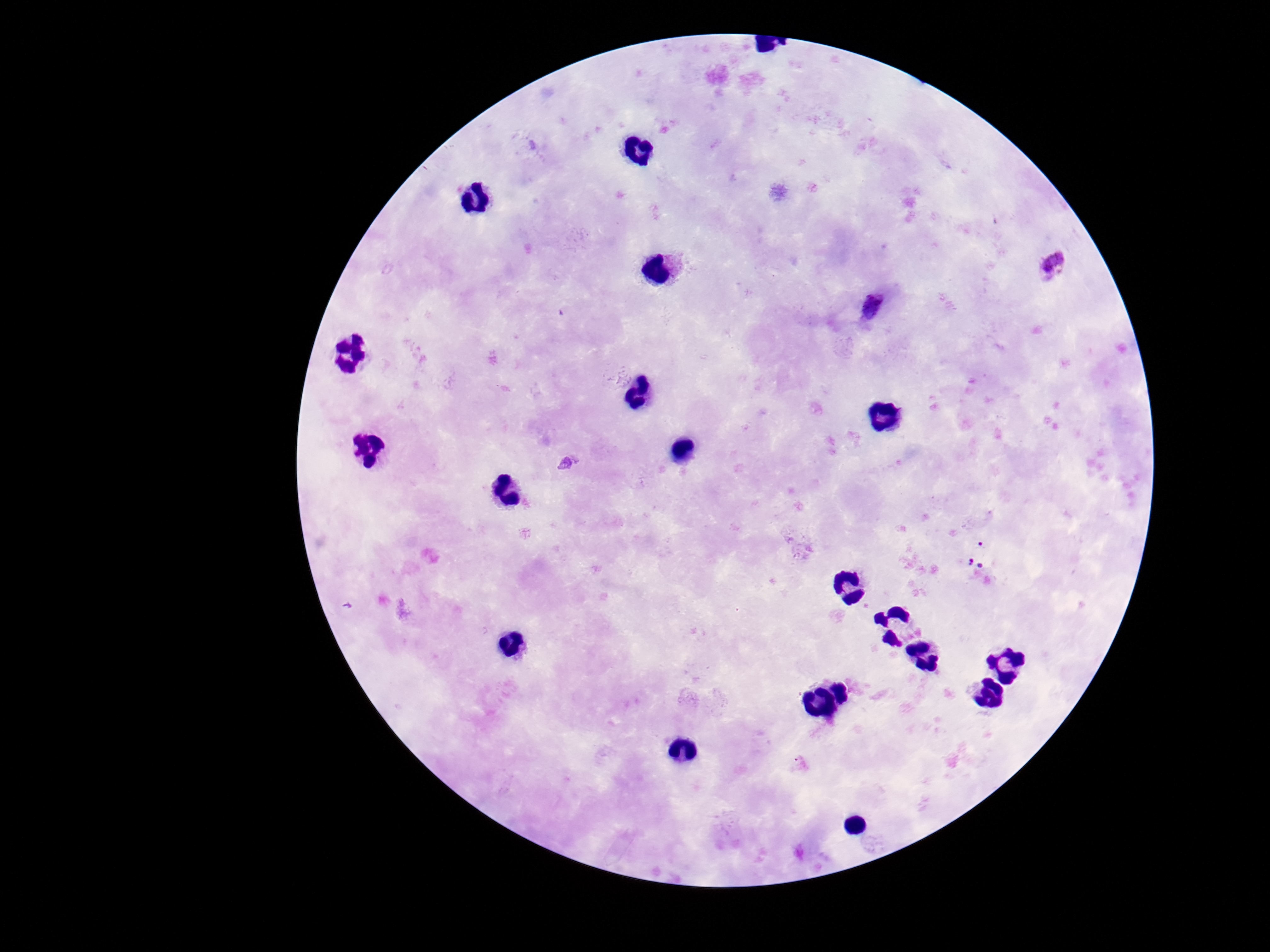

Approximate centers as {x, y} in pixels.
Summary:
  - Plasmodium parasite locations: {1053, 264}, {873, 306}, {567, 463}, {980, 553}
  - Capture: smartphone camera through the microscope eyepiece
  - Preparation: thick blood film
  - Magnification: 100x
  - Stain: Giemsa
  - Patient malaria status: positive
  - Field of view: single
  - Image size: 1270×952 pixels